Report the malaria status of this cell.
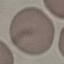
Uninfected.

Summary:
  - Stain: Giemsa
  - Preparation: thin smear
  - Image type: cell patch, automatically extracted from a larger field of view and resized to 64 × 64 pixels
  - Capture: smartphone through the microscope eyepiece